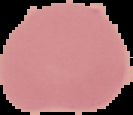
Summary:
  - Result: no Plasmodium parasites detected
  - Image size: 133×115 pixels
  - Preparation: thin blood smear
  - Image type: cell region segmented out of the field of view; surrounding area masked to black